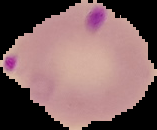
From a thin blood film. Image is 157×130 pixels. Segmented cell region on a black background. Malaria status: parasitized.